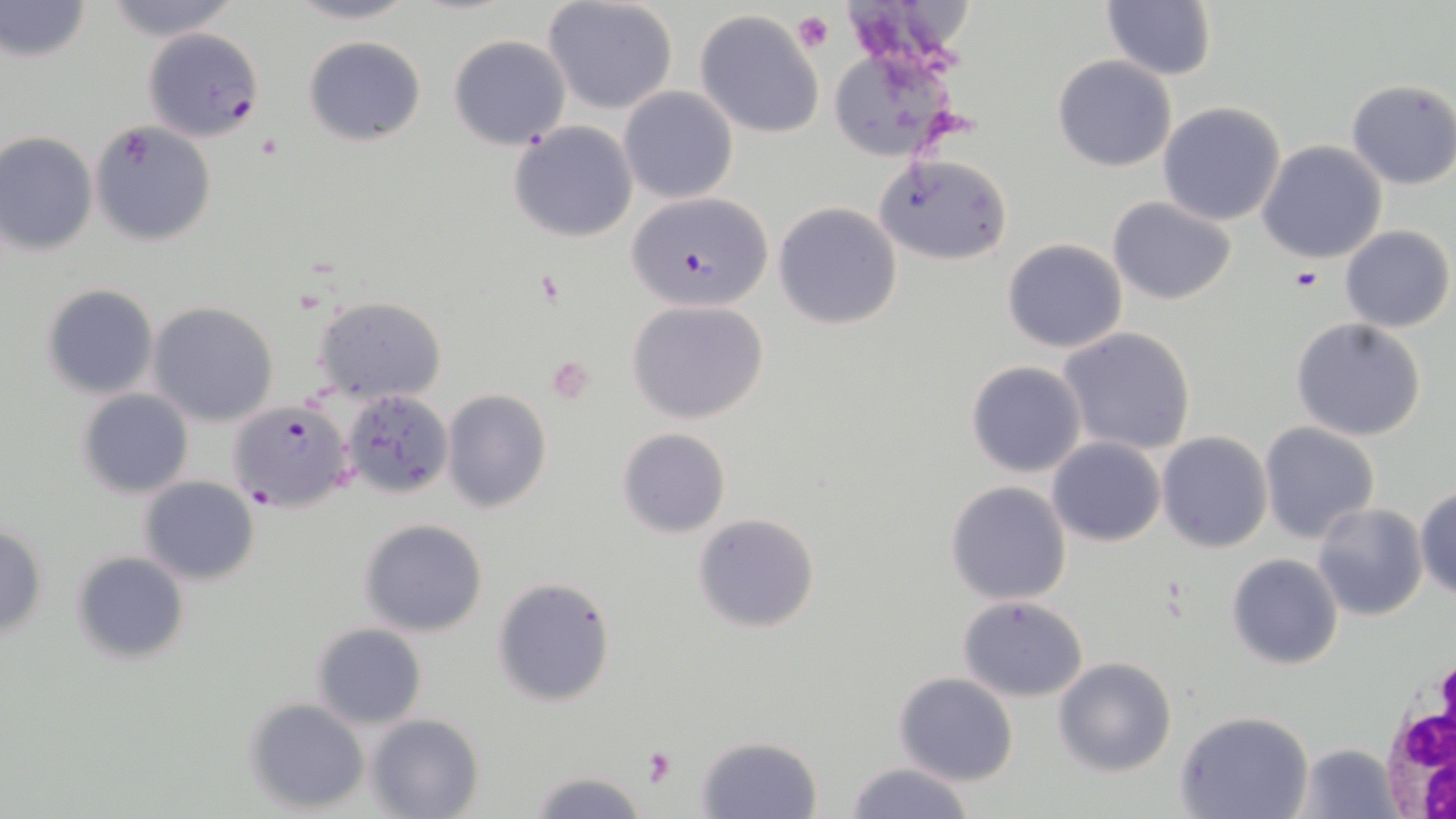

Approximate bounding boxes as (x1, y1, x2, y2) in pixels. Platelet locations: (792, 10, 835, 53), (257, 132, 280, 158), (1289, 266, 1323, 293), (640, 747, 676, 788). Uninfected red blood cell locations: (0, 0, 91, 63), (103, 0, 237, 39), (284, 0, 423, 24), (543, 0, 679, 113), (1100, 0, 1216, 81), (694, 9, 826, 139), (448, 34, 571, 150), (303, 35, 427, 146), (1051, 55, 1177, 173), (1346, 78, 1456, 190), (618, 86, 739, 204), (1158, 101, 1288, 225), (90, 121, 217, 247), (507, 121, 638, 243), (0, 131, 97, 256), (1256, 140, 1388, 264), (874, 153, 1012, 264), (1107, 198, 1238, 305), (774, 201, 903, 330), (1340, 226, 1453, 332), (1003, 239, 1127, 352), (41, 283, 159, 400), (312, 297, 447, 404), (625, 300, 769, 425), (147, 303, 279, 427), (1290, 316, 1427, 442), (1058, 327, 1197, 457), (965, 361, 1086, 477), (340, 387, 454, 500), (77, 389, 193, 498), (442, 389, 552, 513), (1259, 422, 1381, 544), (616, 427, 731, 537), (1157, 431, 1272, 552), (1047, 436, 1164, 546), (139, 476, 260, 586), (944, 481, 1072, 605), (1415, 484, 1456, 601), (1313, 503, 1428, 621), (692, 514, 821, 633), (360, 518, 489, 637), (0, 522, 48, 639), (71, 551, 189, 664), (1227, 554, 1342, 670), (491, 575, 619, 707), (959, 596, 1088, 702), (311, 623, 427, 729), (1053, 656, 1177, 776), (894, 672, 1018, 785), (244, 698, 370, 814), (1177, 709, 1313, 819), (365, 713, 483, 819), (694, 735, 823, 818), (1297, 742, 1400, 817), (843, 762, 977, 819), (527, 769, 649, 818). Plasmodium falciparum-infected red blood cell locations: (143, 27, 264, 141), (626, 190, 774, 314), (226, 401, 355, 512). White blood cell locations: (1367, 659, 1456, 819). Slide-level diagnosis: Plasmodium falciparum. Image is 1456×819 pixels. May-Grünwald-Giemsa-stained preparation. Thin blood smear. One field of a larger specimen. Captured at 1000x magnification. Light microscopy.